State the blood parasite species.
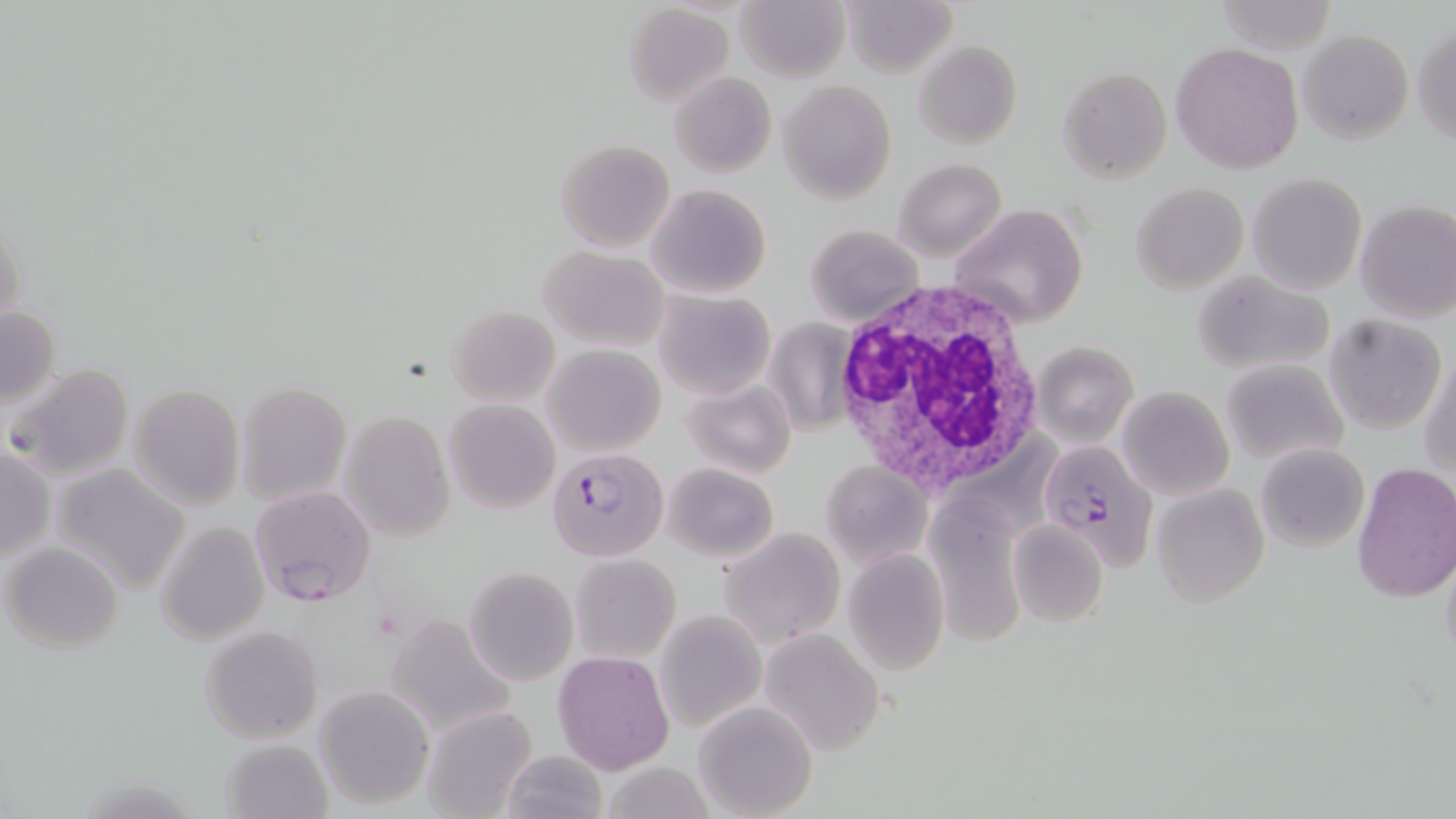

Plasmodium falciparum.

Summary:
  - Coordinate format: approximate bounding boxes as (x1, y1, x2, y2) in pixels
  - White blood cell locations: (828, 277, 1049, 497)
  - Plasmodium falciparum-infected red blood cell locations: (1034, 436, 1165, 572), (549, 448, 667, 562), (250, 485, 378, 608)
  - Uninfected red blood cell locations: (734, 0, 849, 82), (839, 0, 955, 77), (1214, 1, 1337, 54), (623, 3, 733, 106), (1413, 26, 1456, 146), (1299, 30, 1412, 144), (914, 39, 1022, 151), (1171, 41, 1305, 175), (1058, 66, 1172, 183), (669, 72, 777, 178), (779, 79, 896, 205), (554, 137, 676, 253), (895, 158, 1006, 262), (1247, 172, 1368, 295), (649, 183, 770, 300), (1132, 183, 1248, 294), (1354, 200, 1456, 323), (948, 204, 1090, 329), (0, 215, 23, 339), (803, 225, 923, 325), (539, 245, 668, 354), (1191, 270, 1336, 374), (653, 290, 776, 399), (1, 304, 60, 411), (446, 305, 559, 407), (1325, 314, 1448, 434), (764, 318, 860, 434), (1031, 341, 1138, 446), (543, 344, 665, 457), (1420, 350, 1456, 482), (1220, 359, 1349, 465), (6, 362, 136, 480), (682, 377, 795, 479), (237, 380, 352, 505), (129, 383, 245, 510), (1117, 386, 1234, 500), (443, 399, 559, 512), (339, 410, 456, 542), (930, 424, 1062, 548), (1255, 442, 1370, 552), (1, 446, 53, 564), (823, 460, 932, 567), (1353, 461, 1456, 602), (663, 463, 778, 562), (50, 464, 190, 594), (1151, 483, 1270, 605), (925, 493, 1035, 649), (154, 519, 269, 645), (1008, 519, 1108, 628), (721, 527, 845, 649), (3, 542, 123, 653), (1440, 546, 1456, 669), (842, 548, 951, 675), (571, 553, 681, 660), (464, 566, 580, 686), (654, 611, 765, 733), (382, 616, 517, 738), (199, 624, 324, 744), (759, 627, 887, 755), (553, 653, 673, 773), (314, 686, 433, 809), (692, 701, 818, 818), (420, 705, 539, 819), (220, 737, 333, 819), (499, 750, 610, 819), (599, 763, 715, 819)
  - Modality: light microscopy
  - Stain: May-Grünwald-Giemsa
  - Preparation: thin blood smear
  - Field of view: single
  - Magnification: 1000x
  - Image size: 1456×819 pixels